Locate every uninfected red blood cell.
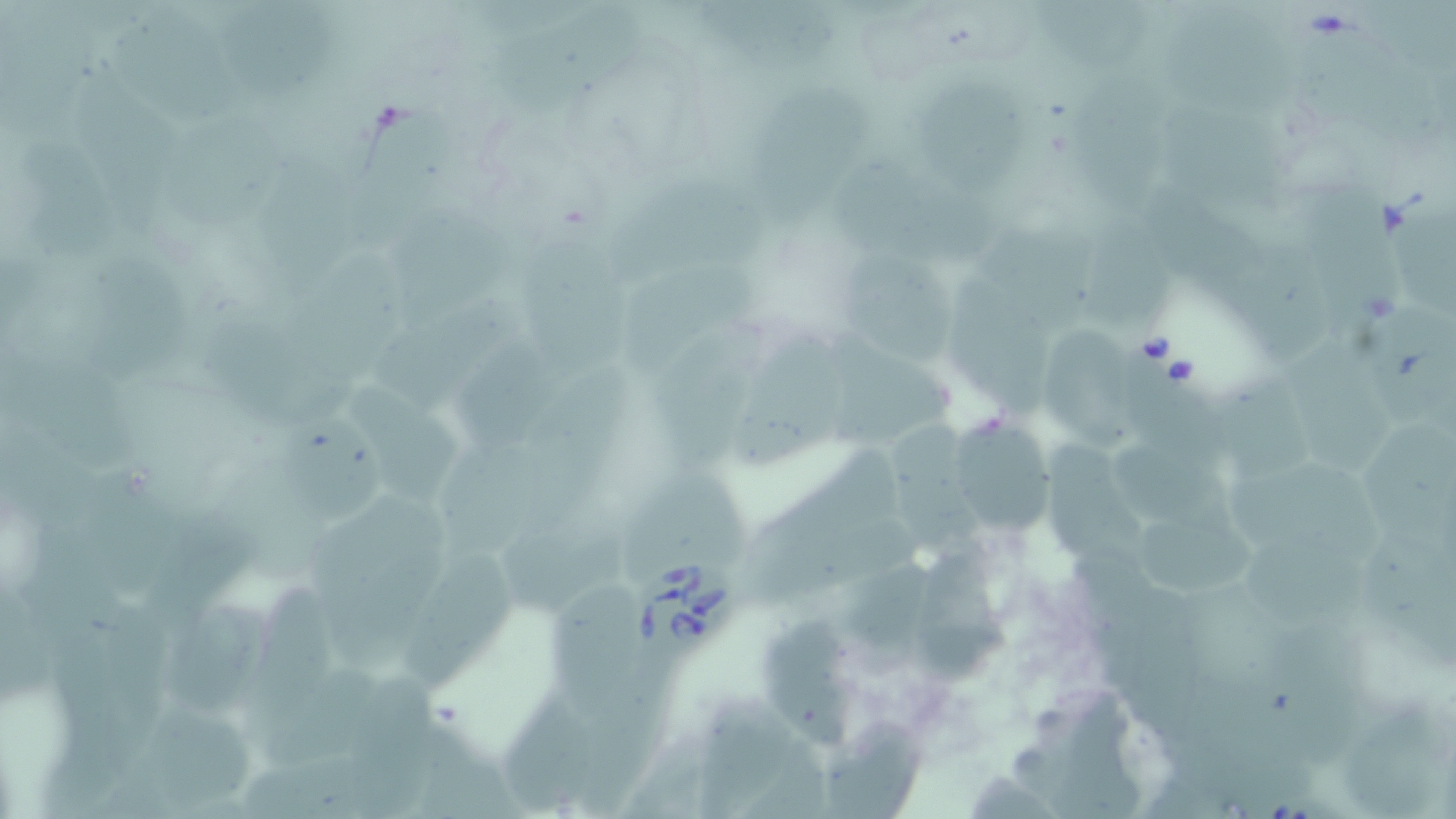
Approximate bounding boxes as (x1,y1)-(x2,y2) corner pairs in pixels.
Uninfected red blood cells: (1164,18)-(1299,117), (1042,22)-(1158,73), (228,23)-(331,100), (12,25)-(98,143), (123,26)-(253,128), (505,26)-(630,117), (706,27)-(859,80), (1312,27)-(1436,159), (83,46)-(185,239), (1075,74)-(1176,214), (902,85)-(1035,180), (772,90)-(874,222), (353,103)-(461,235), (174,104)-(290,229), (1173,106)-(1288,208), (23,139)-(121,267), (267,149)-(358,294), (823,156)-(1007,271), (623,166)-(776,278), (1145,185)-(1274,317), (1292,191)-(1410,329), (1394,202)-(1456,314), (397,206)-(517,340), (521,231)-(634,381), (1098,231)-(1180,336), (988,235)-(1103,332), (1249,240)-(1334,361), (298,245)-(416,373), (837,247)-(959,367), (106,251)-(188,368), (630,251)-(765,367), (952,279)-(1056,418), (371,294)-(517,408), (1377,310)-(1451,427), (205,318)-(347,430), (735,326)-(843,466), (649,330)-(743,464), (1059,330)-(1141,447), (820,332)-(959,460), (1295,340)-(1386,483), (16,344)-(146,475), (468,348)-(552,463), (1134,352)-(1233,483), (536,360)-(623,517), (1217,371)-(1319,485), (347,373)-(464,509), (879,419)-(981,558), (961,419)-(1062,549), (294,423)-(385,528), (1370,424)-(1453,552), (438,438)-(544,554), (760,448)-(900,544), (1123,454)-(1237,548), (1048,455)-(1150,581), (1236,466)-(1398,580), (83,476)-(169,609), (633,476)-(748,582), (323,491)-(437,601), (158,499)-(257,640), (20,507)-(150,645), (512,509)-(635,607), (757,509)-(928,616), (1141,519)-(1258,596), (1369,525)-(1449,662), (1241,531)-(1375,635), (413,540)-(527,686), (906,549)-(1009,699), (335,550)-(461,664), (1077,550)-(1203,666), (837,552)-(945,663), (249,585)-(338,730), (560,595)-(658,707), (181,616)-(280,715), (765,619)-(863,745), (48,643)-(169,805), (1266,645)-(1363,772), (276,656)-(394,758), (1115,660)-(1252,749), (576,680)-(668,818), (340,682)-(441,816), (503,687)-(603,809), (153,695)-(252,804), (700,696)-(794,816), (1337,696)-(1453,813), (816,717)-(920,819), (609,719)-(720,818), (430,729)-(527,816), (1178,729)-(1306,810), (752,742)-(841,814).

Babesia divergens-infected red blood cell locations: (625,560)-(744,663). Slide-level diagnosis: Babesia divergens. One field of a larger specimen. May-Grünwald-Giemsa-stained preparation. 1000x magnification. Thin blood smear. Light microscopy. Image is 1456×819 pixels.